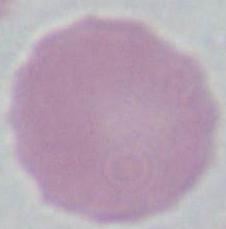

Photomicrograph. Captured at 1000x magnification. An erythrocyte is seen.